Give the position of every leukocyte visible.
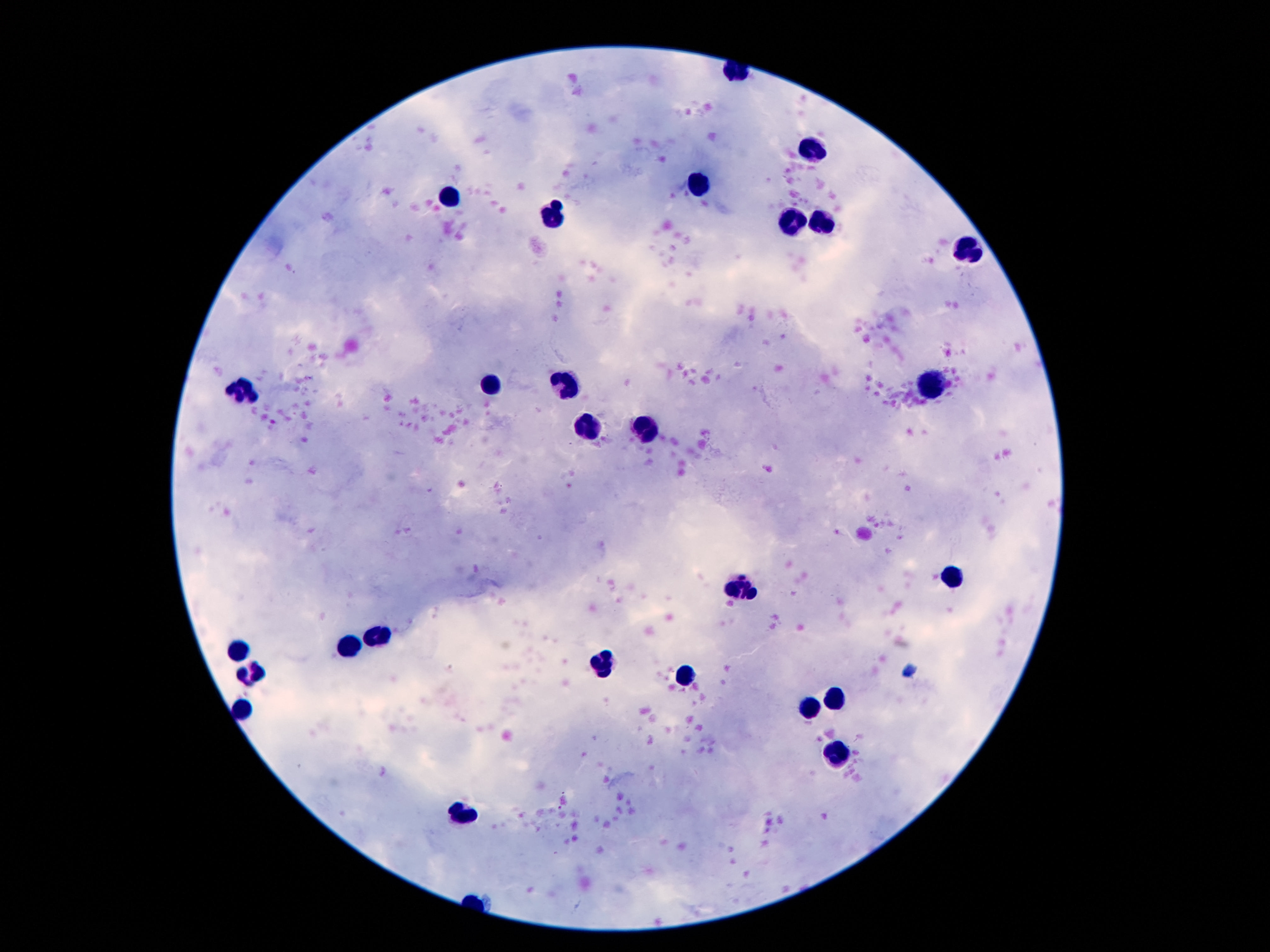

Approximate object centers, in pixels from the top-left corner.
Leukocytes: (x=815, y=148), (x=700, y=184), (x=446, y=193), (x=557, y=216), (x=819, y=221), (x=792, y=222), (x=970, y=250), (x=486, y=382), (x=565, y=384), (x=931, y=386), (x=246, y=392), (x=591, y=424), (x=641, y=428), (x=952, y=577), (x=738, y=588), (x=377, y=636), (x=349, y=645), (x=240, y=648), (x=603, y=662), (x=251, y=669), (x=687, y=678), (x=840, y=697), (x=244, y=704), (x=809, y=706), (x=836, y=756), (x=463, y=813).

stain: Giemsa
preparation: thick blood film
patient_malaria_status: not infected
image_size: 1270×952 pixels
capture: smartphone camera through the microscope eyepiece
field_of_view: one from this slide
magnification: 100x